Give the position of every leukocyte.
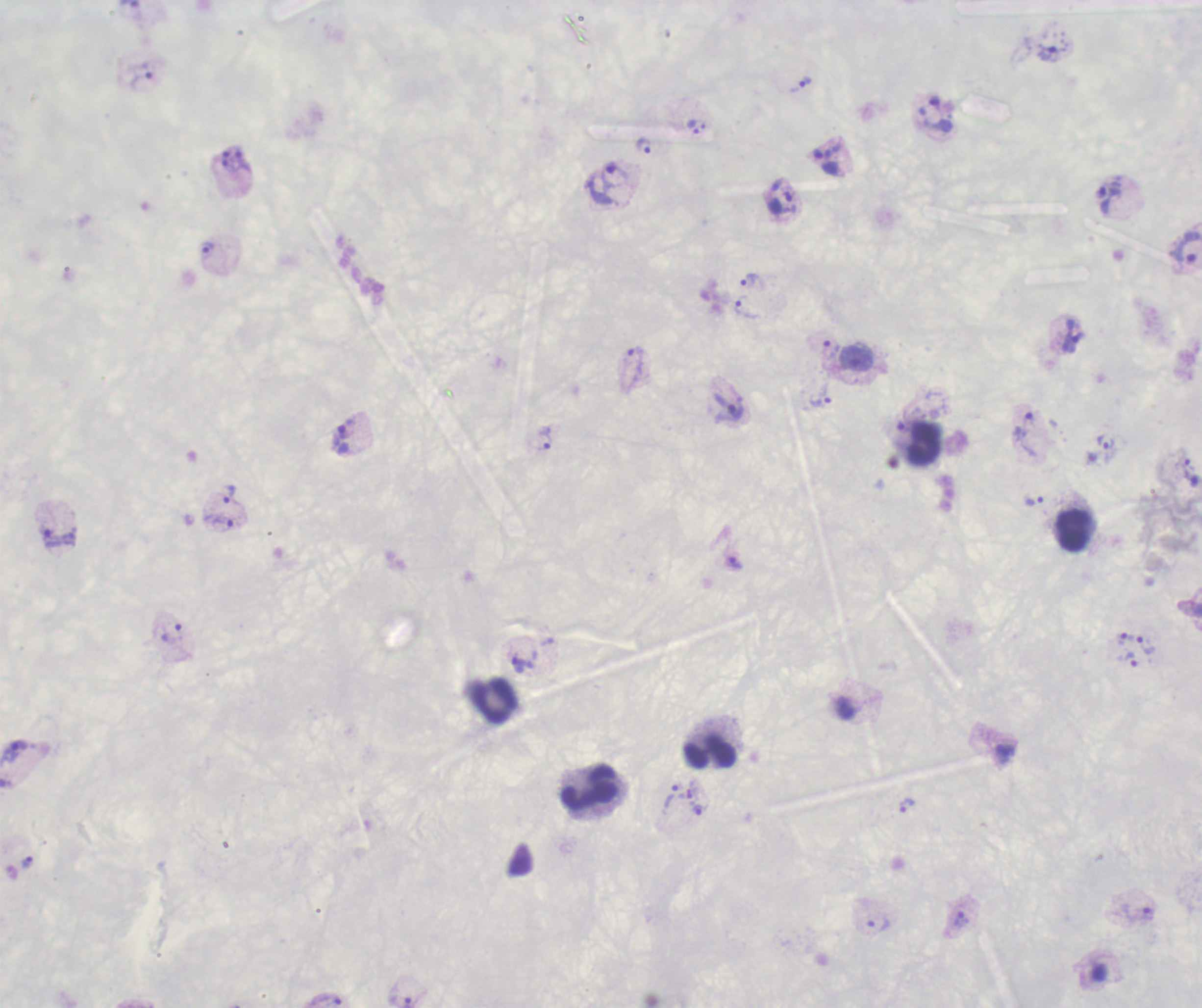
Approximate centers as (x, y) in pixels.
Leukocytes: (925, 446), (1072, 531), (490, 702), (709, 754), (591, 787).

Approximate centers as (x, y) in pixels.
Summary:
  - Trophozoite locations: (141, 80), (797, 83), (695, 128), (643, 145), (243, 162), (614, 177), (1108, 196), (208, 249), (1184, 249), (751, 282), (744, 310), (1070, 336), (830, 349), (636, 367), (819, 400), (729, 408), (1026, 432), (543, 439), (1106, 441), (1185, 465), (228, 495), (1034, 502), (219, 521), (50, 539), (735, 564), (171, 633), (1124, 637), (1145, 646), (1129, 660), (524, 664), (13, 750), (672, 796), (905, 805), (697, 808), (27, 862), (1136, 912), (959, 918), (877, 923), (406, 999), (326, 1000)
  - Stain: Romanowsky
  - Result: positive for Plasmodium parasites
  - Background quality: unsatisfactory
  - Field of view: single
  - Preparation: thick smear of blood
  - Image size: 1202×1008 pixels
  - Context: previously used in an actual diagnosis
  - Magnification: 100x